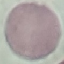

{
  "result": "no malaria parasites detected",
  "capture": "smartphone through the microscope eyepiece",
  "preparation": "thin blood film",
  "image_type": "automatically extracted cell patch, resized to 64 × 64 pixels",
  "stain": "Giemsa"
}